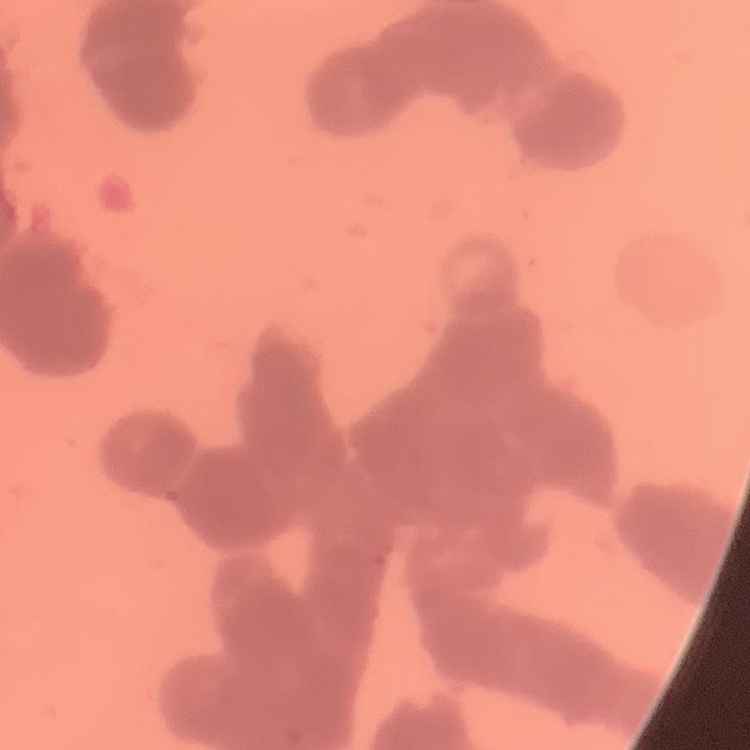
Summary:
  - Erythrocyte morphology: rouleaux formation
  - Image type: one tile cut from a larger photomicrograph
  - Stain: Field's or Giemsa
  - Preparation: thin blood smear